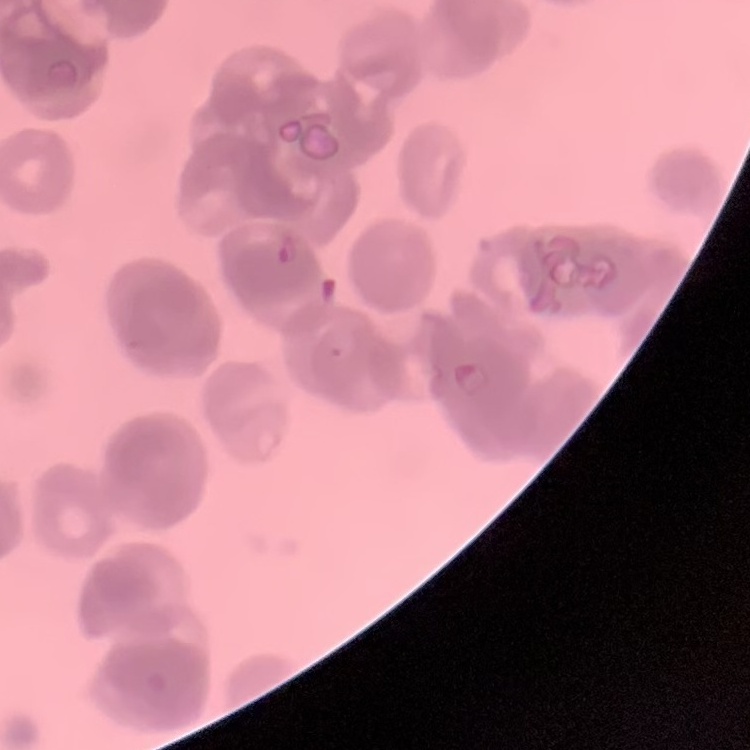
red blood cell morphology = rouleaux formation
preparation = thin blood smear
stain = Field's or Giemsa
image type = one tile cut from a larger photomicrograph